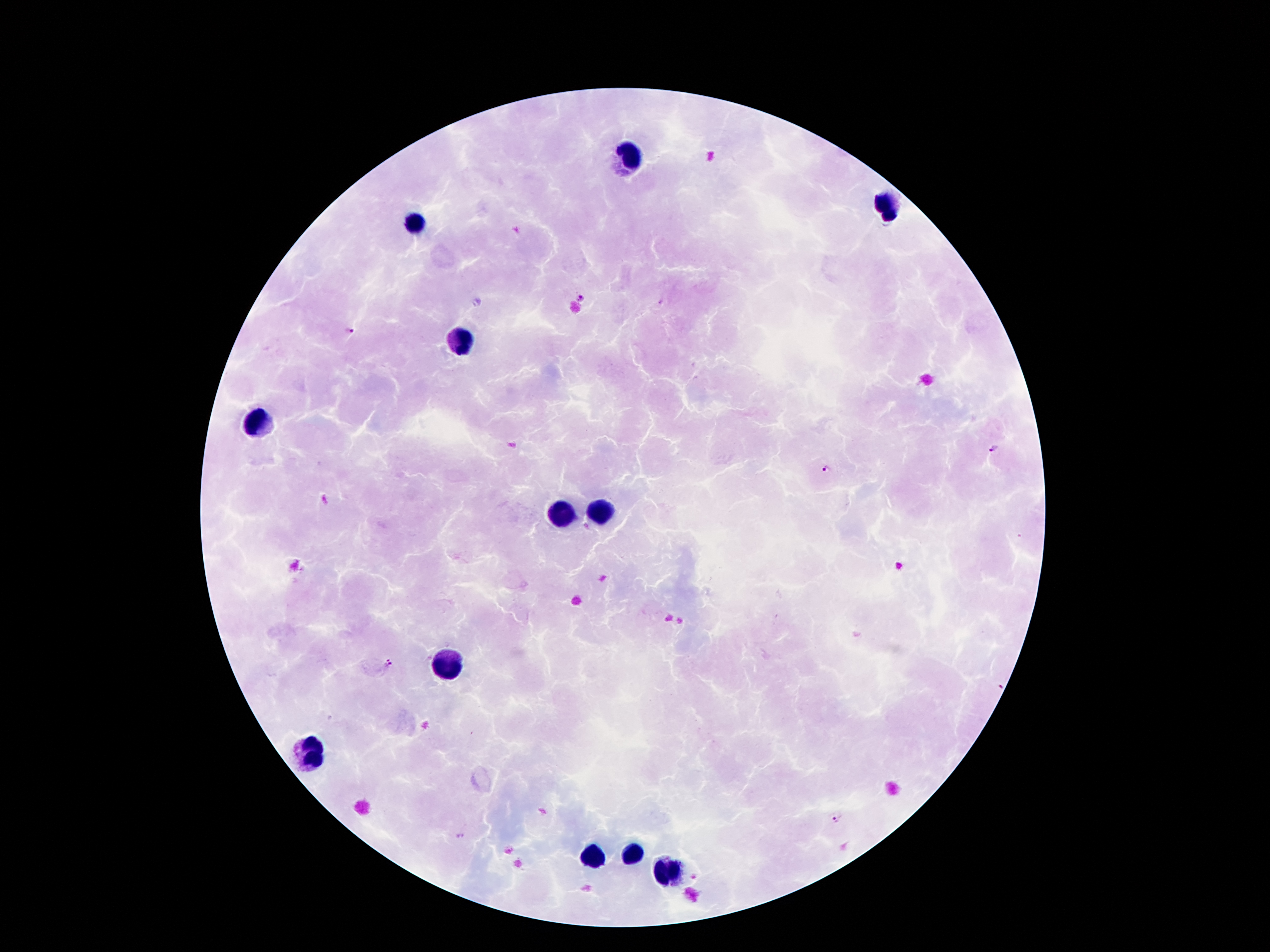

Approximate object centers, in pixels from the top-left corner. Malaria parasite locations: (x=583, y=298), (x=349, y=329), (x=991, y=448), (x=828, y=470), (x=388, y=661), (x=836, y=818), (x=459, y=836). Leukocyte locations: (x=628, y=154), (x=884, y=202), (x=416, y=221), (x=462, y=343), (x=260, y=420), (x=559, y=513), (x=598, y=513), (x=449, y=666), (x=313, y=752), (x=628, y=851), (x=590, y=859), (x=670, y=874). Giemsa stain. Photographed through the microscope eyepiece with a smartphone camera. Image is 1270×952 pixels. Thick blood film. Patient malaria status: positive for Plasmodium falciparum. Single field of view. 100x magnification.